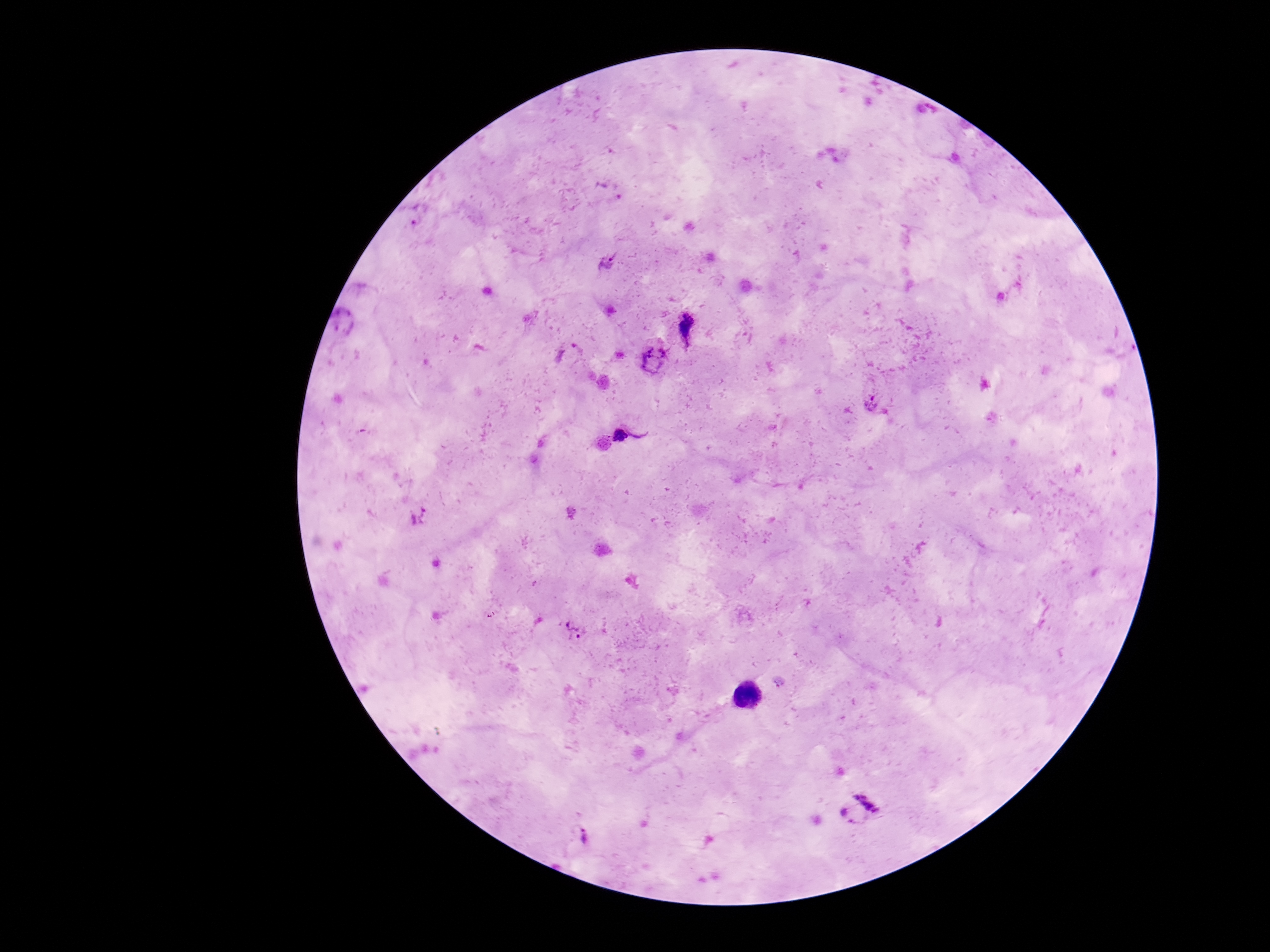 Approximate centers as {x, y} in pixels. Plasmodium parasite locations: {607, 264}, {689, 325}, {567, 353}, {655, 359}, {869, 403}, {620, 435}, {571, 512}, {418, 516}, {573, 632}, {858, 808}, {582, 838}. Image is 1270×952 pixels. Thick blood smear. Patient malaria status: positive. One field from this slide. 100x magnification. Photographed through the microscope eyepiece with a smartphone camera. Giemsa stain.